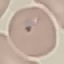

Malaria status: uninfected. Automatically extracted cell patch, resized to 64 × 64 pixels. Thin blood film. Giemsa-stained preparation. Photographed with a smartphone camera at the microscope eyepiece.